State which parasite is depicted.
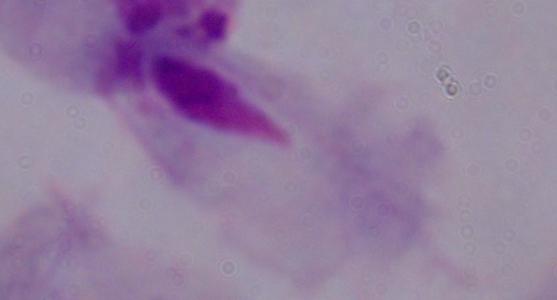

This is a trichomonad.

modality = micrograph
magnification = 1000x